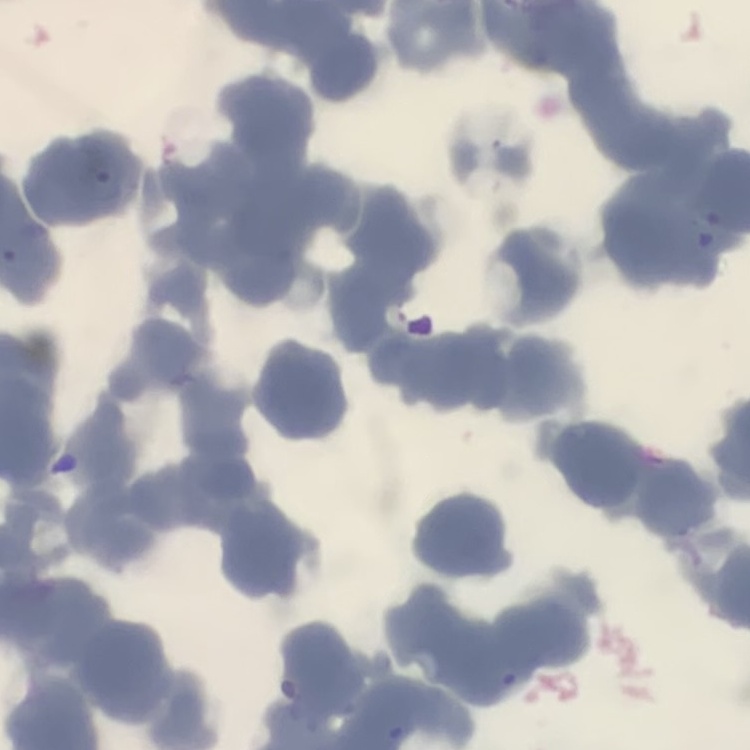

Summary:
  - Red blood cell morphology: rouleaux formation
  - Preparation: thin peripheral smear
  - Image type: one tile cut from a larger photomicrograph
  - Stain: Field's or Giemsa